Name the parasite shown.
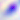

This is Toxoplasma gondii.

Summary:
  - Magnification: 400x
  - Modality: micrograph